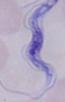

identification: trypanosome
modality: micrograph
magnification: 1000x